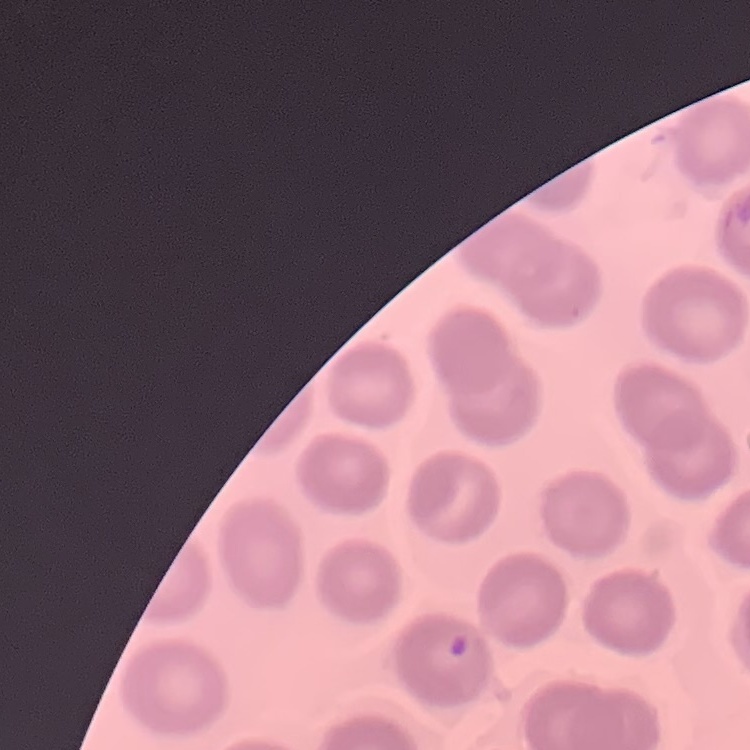 The red blood cells show no rouleaux formation. One tile cut from a larger photomicrograph. Thin blood smear. Field's or Giemsa stain.